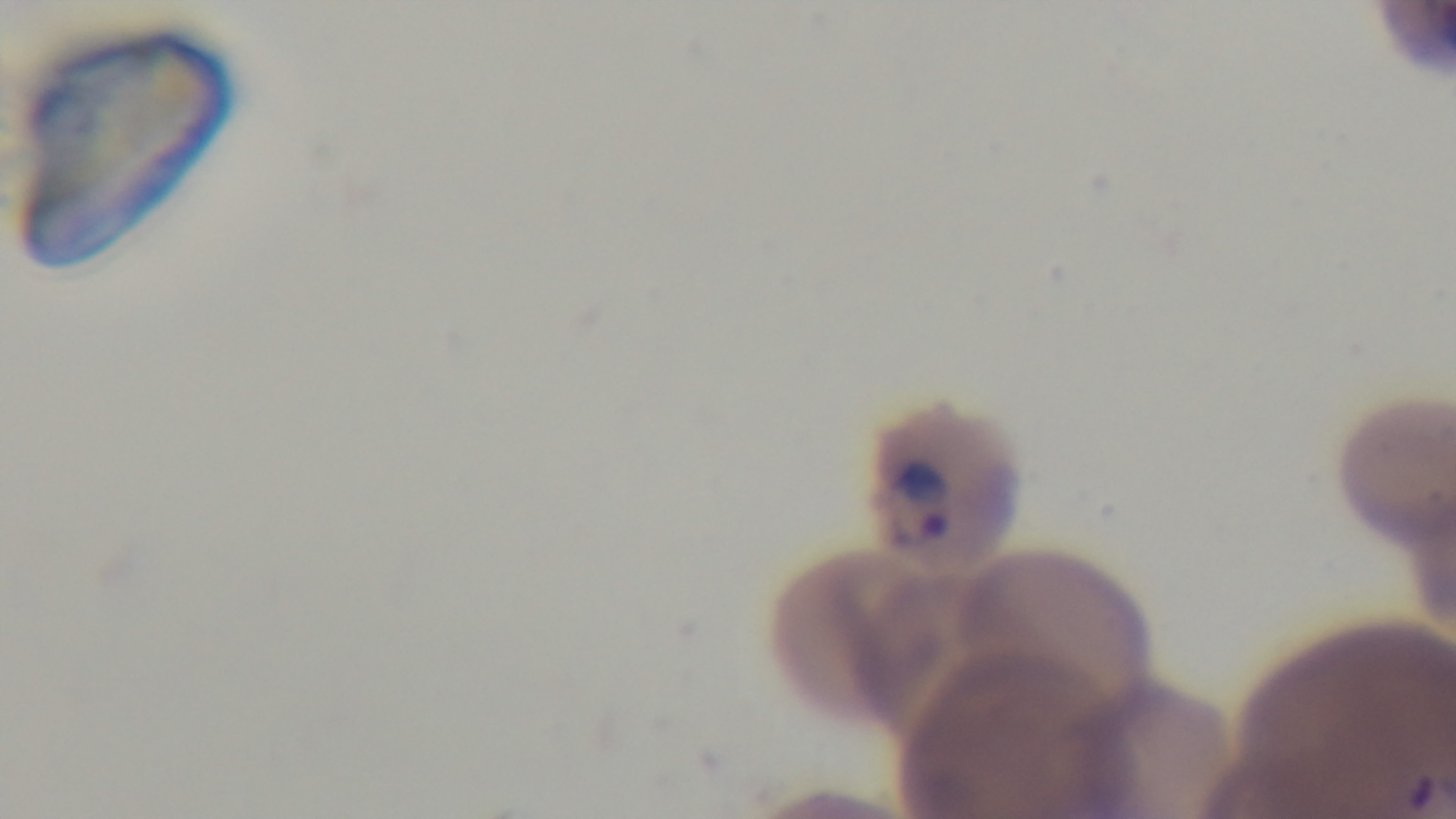

Summary:
  - Capture: mounted 4K digital camera
  - Preparation: thin smear
  - Modality: light microscopy
  - Malaria status: infected
  - Stain: Giemsa
  - Field of view: single
  - Objective: 100x oil immersion